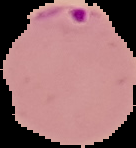
preparation = thin blood smear
image size = 136×148 pixels
image type = cell region segmented out of the field of view; surrounding area masked to black
result = Plasmodium parasites detected